Name the parasite shown.
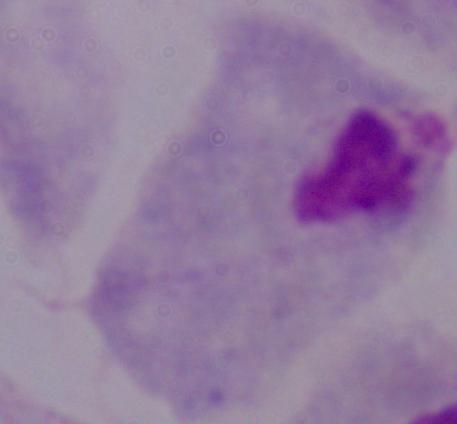

This is a trichomonad.

1000x magnification. Photomicrograph.